Locate and identify every blood parasite.
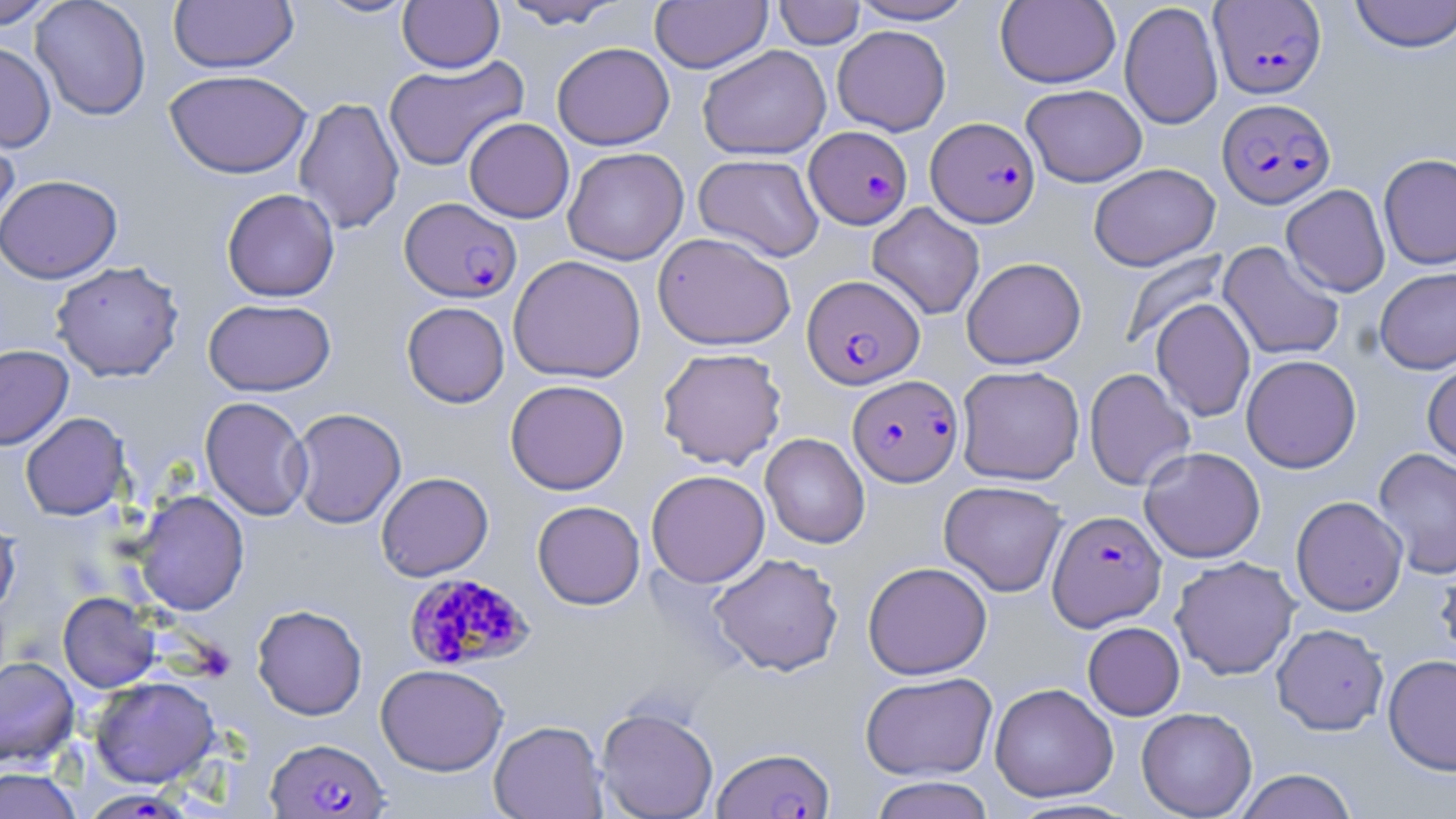

Approximate bounding boxes as named x1/y1/x2/y2 corners in pixels.
Plasmodium falciparum-infected red blood cells: (x1=1210, y1=1, x2=1326, y2=99), (x1=1217, y1=98, x2=1336, y2=208), (x1=926, y1=117, x2=1040, y2=227), (x1=805, y1=126, x2=912, y2=229), (x1=400, y1=197, x2=522, y2=302), (x1=802, y1=274, x2=925, y2=390), (x1=848, y1=374, x2=962, y2=487), (x1=1048, y1=509, x2=1166, y2=630), (x1=404, y1=572, x2=533, y2=672), (x1=266, y1=737, x2=390, y2=818), (x1=713, y1=746, x2=835, y2=819), (x1=90, y1=793, x2=196, y2=819).
No Plasmodium ovale, Plasmodium malariae, Plasmodium vivax, Babesia divergens, or Trypanosoma brucei observed.

Uninfected red blood cell locations: (x1=0, y1=0, x2=59, y2=29), (x1=31, y1=0, x2=151, y2=121), (x1=168, y1=0, x2=298, y2=73), (x1=314, y1=0, x2=419, y2=19), (x1=398, y1=0, x2=504, y2=73), (x1=499, y1=0, x2=627, y2=29), (x1=649, y1=0, x2=773, y2=73), (x1=847, y1=0, x2=979, y2=24), (x1=995, y1=0, x2=1120, y2=88), (x1=1348, y1=0, x2=1456, y2=53), (x1=773, y1=1, x2=865, y2=49), (x1=1119, y1=2, x2=1223, y2=130), (x1=832, y1=25, x2=951, y2=136), (x1=0, y1=41, x2=56, y2=153), (x1=552, y1=42, x2=674, y2=150), (x1=697, y1=45, x2=831, y2=160), (x1=384, y1=55, x2=529, y2=172), (x1=164, y1=69, x2=312, y2=179), (x1=1021, y1=84, x2=1147, y2=187), (x1=293, y1=97, x2=405, y2=235), (x1=464, y1=117, x2=574, y2=222), (x1=0, y1=120, x2=21, y2=240), (x1=562, y1=147, x2=689, y2=265), (x1=693, y1=153, x2=825, y2=262), (x1=1378, y1=153, x2=1456, y2=270), (x1=1088, y1=162, x2=1220, y2=271), (x1=0, y1=174, x2=122, y2=283), (x1=1281, y1=184, x2=1390, y2=297), (x1=221, y1=188, x2=340, y2=302), (x1=867, y1=202, x2=985, y2=320), (x1=653, y1=232, x2=796, y2=351), (x1=1218, y1=241, x2=1345, y2=362), (x1=1119, y1=248, x2=1232, y2=351), (x1=508, y1=255, x2=646, y2=383), (x1=962, y1=257, x2=1086, y2=370), (x1=51, y1=261, x2=184, y2=382), (x1=1375, y1=267, x2=1456, y2=374), (x1=203, y1=298, x2=336, y2=396), (x1=1151, y1=298, x2=1255, y2=422), (x1=402, y1=301, x2=509, y2=407), (x1=0, y1=344, x2=73, y2=450), (x1=657, y1=347, x2=787, y2=469), (x1=1241, y1=354, x2=1361, y2=473), (x1=1422, y1=360, x2=1456, y2=468), (x1=956, y1=365, x2=1085, y2=485), (x1=1083, y1=368, x2=1196, y2=491), (x1=505, y1=379, x2=630, y2=495), (x1=200, y1=396, x2=312, y2=521), (x1=288, y1=407, x2=406, y2=529), (x1=20, y1=412, x2=131, y2=521), (x1=760, y1=433, x2=870, y2=548), (x1=1139, y1=446, x2=1266, y2=562), (x1=1373, y1=448, x2=1456, y2=579), (x1=646, y1=469, x2=770, y2=588), (x1=376, y1=472, x2=493, y2=581), (x1=938, y1=480, x2=1068, y2=597), (x1=134, y1=490, x2=249, y2=616), (x1=1291, y1=495, x2=1408, y2=616), (x1=532, y1=500, x2=645, y2=609), (x1=0, y1=512, x2=21, y2=617), (x1=708, y1=552, x2=844, y2=676), (x1=1170, y1=556, x2=1301, y2=680), (x1=1435, y1=556, x2=1456, y2=671), (x1=862, y1=561, x2=992, y2=680), (x1=58, y1=592, x2=159, y2=692), (x1=252, y1=604, x2=367, y2=720), (x1=1082, y1=621, x2=1185, y2=720), (x1=1271, y1=623, x2=1389, y2=735), (x1=1382, y1=654, x2=1456, y2=775), (x1=0, y1=655, x2=80, y2=768), (x1=376, y1=663, x2=508, y2=776), (x1=860, y1=671, x2=998, y2=781), (x1=90, y1=676, x2=219, y2=788), (x1=989, y1=682, x2=1118, y2=803), (x1=596, y1=706, x2=719, y2=819), (x1=1136, y1=707, x2=1257, y2=818), (x1=489, y1=720, x2=608, y2=819), (x1=0, y1=766, x2=83, y2=819), (x1=1234, y1=769, x2=1358, y2=819), (x1=869, y1=776, x2=996, y2=819). Slide-level diagnosis: Plasmodium falciparum. Thin blood smear. Image is 1456×819 pixels. Optical microscopy. Single field of view. 1000x magnification. May-Grünwald-Giemsa-stained preparation.